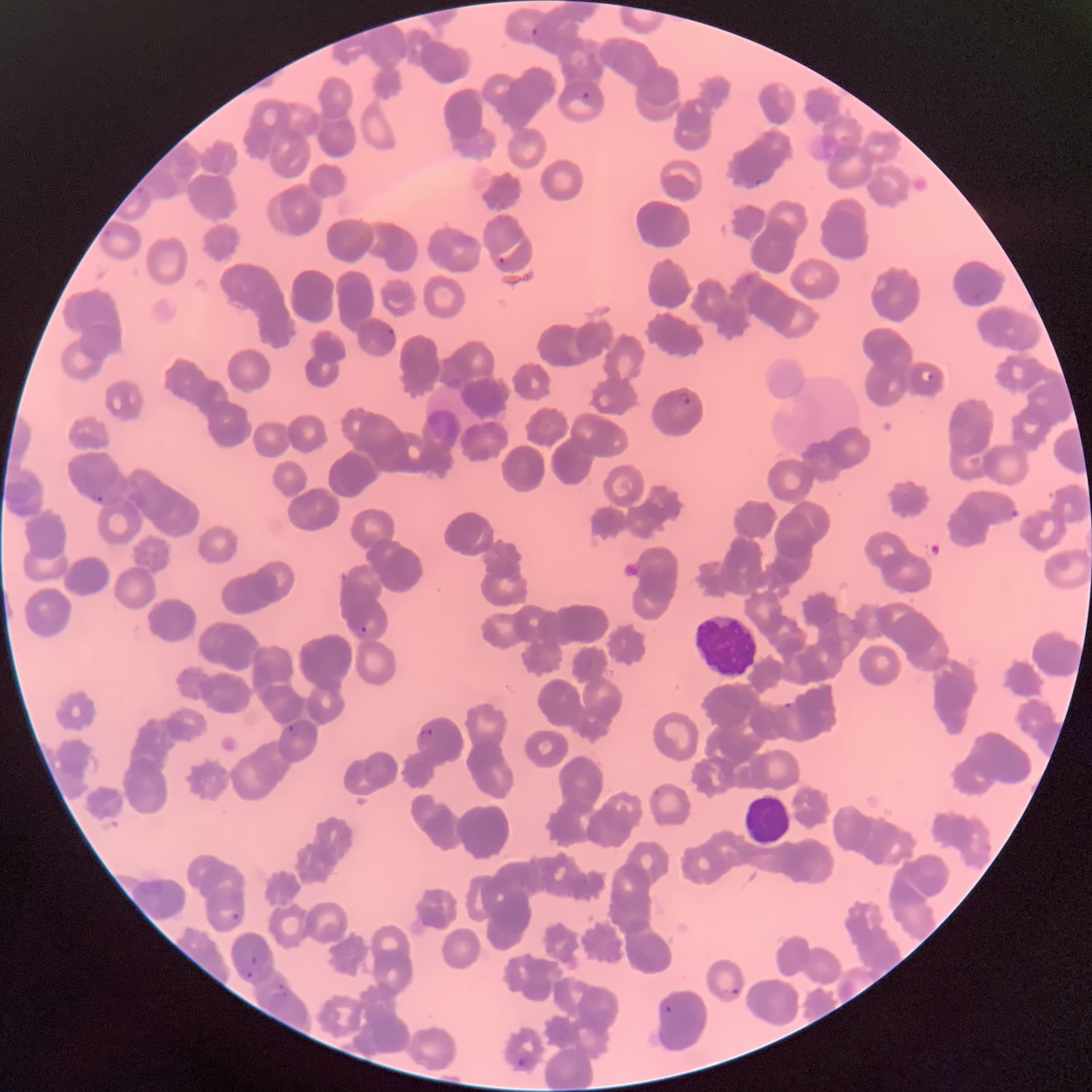

Summary:
  - Coordinate format: approximate bounding boxes as (x1,y1)-(x2,y2) corner pairs in pixels
  - Plasmodium parasite locations: (529,26)-(540,38), (580,90)-(592,102), (753,177)-(764,189), (497,256)-(508,267), (386,326)-(396,338), (920,369)-(934,384), (673,390)-(691,407), (92,492)-(103,502), (357,625)-(368,638), (783,701)-(794,711), (288,721)-(301,737), (419,727)-(434,738), (231,911)-(242,924), (249,954)-(261,966), (245,970)-(253,981), (277,981)-(287,990), (730,987)-(741,997), (278,990)-(290,999), (663,1003)-(674,1015), (516,1055)-(528,1068)
  - White blood cell locations: (692,612)-(760,680), (741,793)-(792,847)
  - Red blood cell morphology: rouleaux formation
  - Preparation: thin blood smear
  - Image size: 1092×1092 pixels
  - Modality: optical microscopy